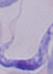

magnification: 1000x
modality: photomicrograph
identification: trypanosome